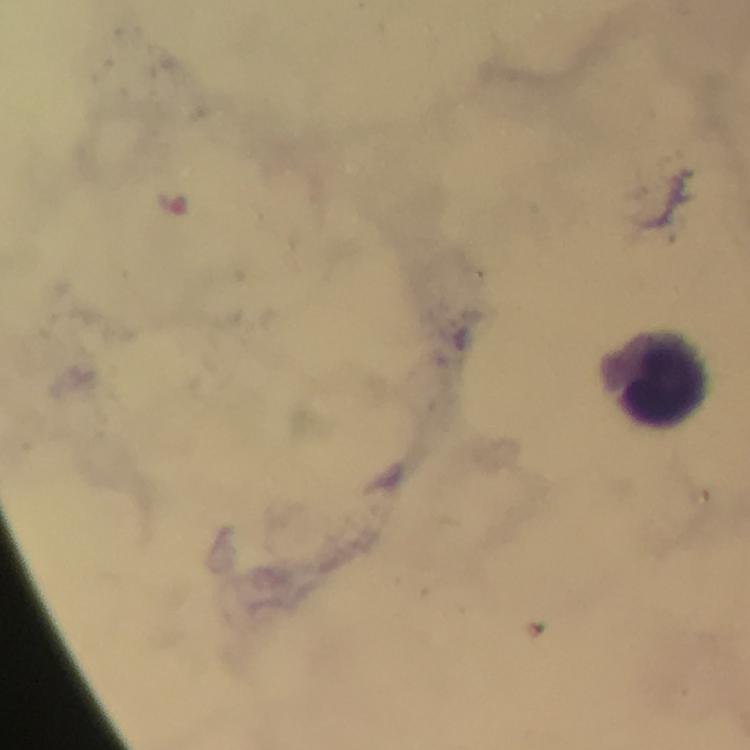
Approximate object centers, in pixels from the top-left corner. Leukocyte locations: (x=661, y=381). Immersion oil applied. Photographed through the microscope with a smartphone camera. Thick blood smear. Giemsa-stained preparation. 100x magnification. Malaria parasites: none seen. From a malaria diagnostic workup. Image is 750×750 pixels. Cropped region of a single field of view.